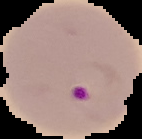
result = malaria parasites detected
preparation = thin blood film
image type = segmented cell region with the area outside set to black
image size = 142×139 pixels